Assess this cell for malaria.
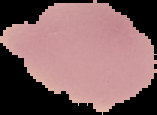
Uninfected.

Summary:
  - Image type: cell region segmented out of the field of view; surrounding area masked to black
  - Preparation: thin blood smear
  - Image size: 157×115 pixels